Give the position of every malaria parasite.
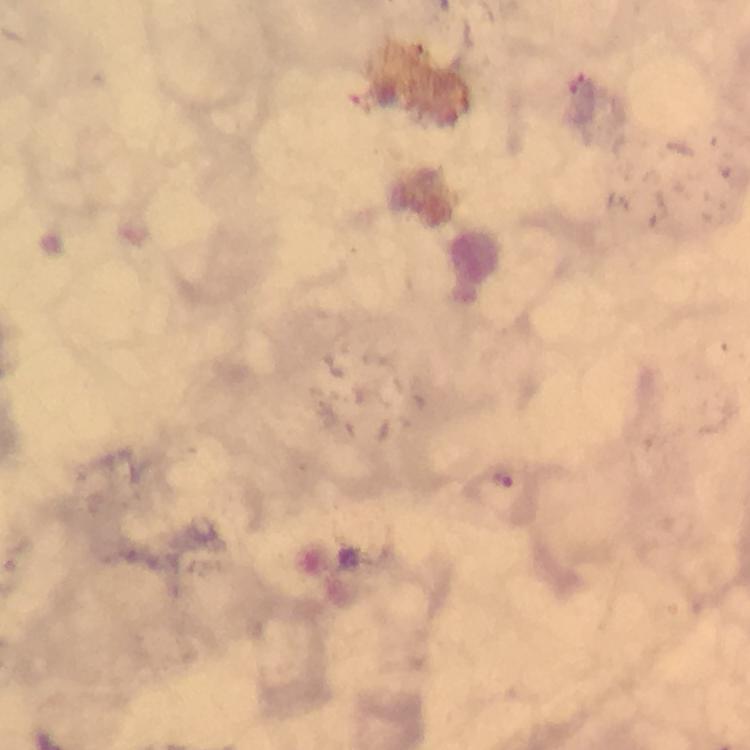
Approximate centers as (x, y) in pixels.
Malaria parasites: (502, 478).

Summary:
  - Magnification: 100x
  - Image size: 750×750 pixels
  - Preparation: thick blood film
  - Cropped from: one field of view
  - Context: from a malaria diagnostic workup
  - Capture: smartphone photograph through a microscope
  - Stain: Giemsa
  - Immersion oil: used